Assess this cell for malaria.
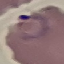

It is parasitized.

Summary:
  - Image type: automatically extracted cell patch, resized to 64 × 64 pixels
  - Capture: smartphone camera at the microscope eyepiece
  - Stain: Giemsa
  - Preparation: thin smear